Identify the parasite.
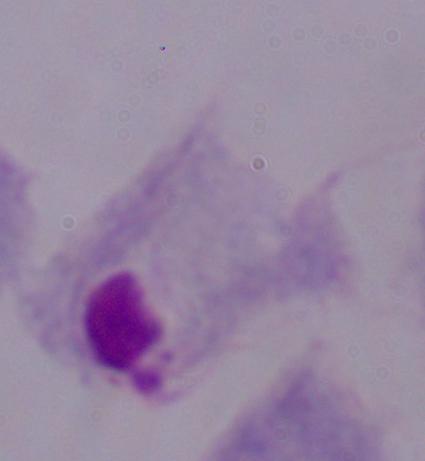

This is a trichomonad.

Summary:
  - Magnification: 1000x
  - Modality: micrograph